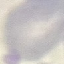

result = negative for malaria parasites
image type = automatically extracted cell patch, resized to 64 × 64 pixels
stain = Giemsa
preparation = thin blood smear
capture = smartphone through the microscope eyepiece